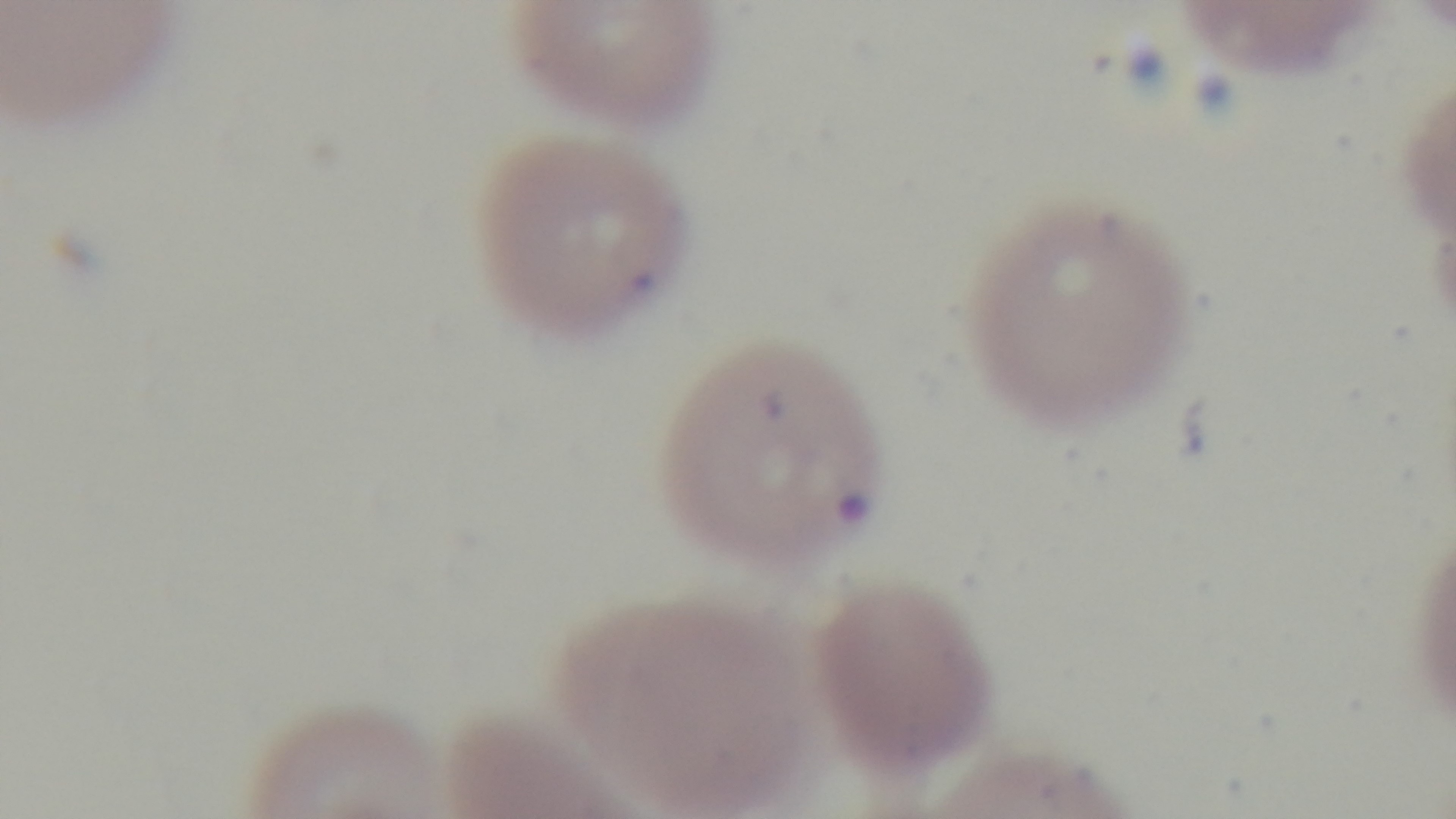
Single field of view. Malaria status: infected. Preparation: thin smear. 100x oil-immersion objective. Light microscopy. Captured with a mounted 4K digital camera. Giemsa-stained.